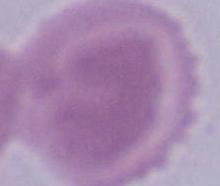

magnification = 1000x
identification = erythrocyte
modality = micrograph